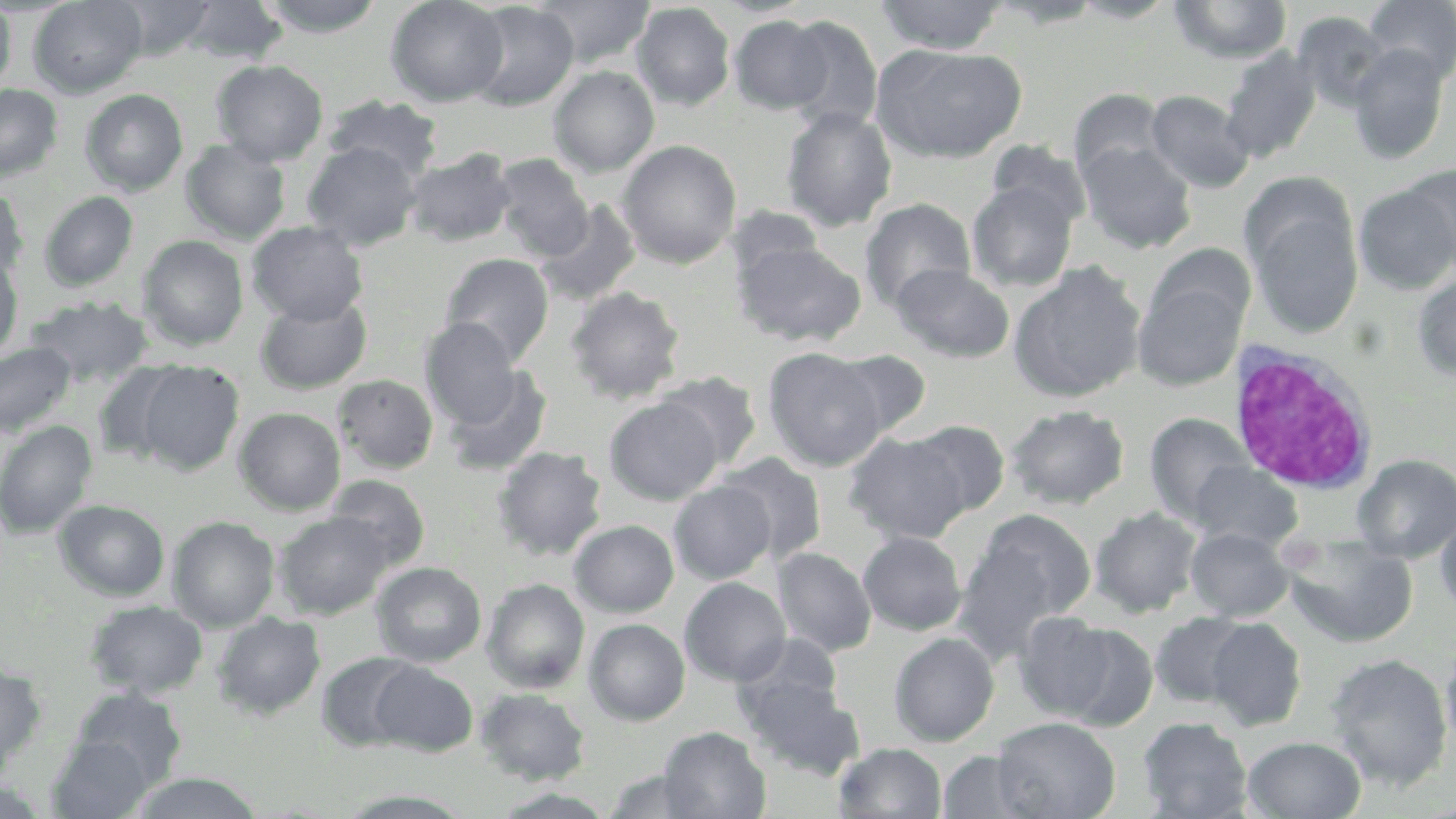
{
  "slide_level_diagnosis": "negative for blood parasites",
  "modality": "optical microscopy",
  "white_blood_cell_locations": "approximate bounding boxes as named x1/y1/x2/y2 corners in pixels: (x1=1226, y1=343, x2=1379, y2=496)",
  "preparation": "thin blood film",
  "stain": "May-Grünwald-Giemsa",
  "image_size": "1456×819 pixels",
  "field_of_view": "single",
  "uninfected_red_blood_cell_locations": "approximate bounding boxes as named x1/y1/x2/y2 corners in pixels: (x1=28, y1=0, x2=147, y2=98), (x1=112, y1=0, x2=218, y2=60), (x1=181, y1=0, x2=289, y2=65), (x1=256, y1=0, x2=386, y2=37), (x1=385, y1=0, x2=509, y2=107), (x1=534, y1=0, x2=655, y2=69), (x1=709, y1=0, x2=815, y2=18), (x1=874, y1=0, x2=1008, y2=54), (x1=1069, y1=0, x2=1181, y2=23), (x1=1361, y1=0, x2=1456, y2=87), (x1=986, y1=1, x2=1106, y2=28), (x1=1169, y1=1, x2=1292, y2=64), (x1=0, y1=2, x2=16, y2=96), (x1=465, y1=2, x2=579, y2=111), (x1=632, y1=2, x2=735, y2=110), (x1=1292, y1=12, x2=1391, y2=111), (x1=729, y1=15, x2=831, y2=114), (x1=783, y1=15, x2=883, y2=135), (x1=872, y1=43, x2=1025, y2=164), (x1=1347, y1=44, x2=1450, y2=165), (x1=1219, y1=46, x2=1322, y2=164), (x1=211, y1=59, x2=329, y2=166), (x1=548, y1=65, x2=659, y2=177), (x1=0, y1=83, x2=63, y2=183), (x1=1069, y1=87, x2=1167, y2=182), (x1=79, y1=89, x2=189, y2=196), (x1=1146, y1=89, x2=1255, y2=194), (x1=323, y1=94, x2=444, y2=182), (x1=780, y1=106, x2=898, y2=232), (x1=180, y1=140, x2=291, y2=244), (x1=302, y1=140, x2=423, y2=250), (x1=617, y1=140, x2=741, y2=269), (x1=986, y1=140, x2=1092, y2=231), (x1=1077, y1=140, x2=1197, y2=254), (x1=405, y1=148, x2=516, y2=247), (x1=491, y1=154, x2=593, y2=263), (x1=1398, y1=164, x2=1456, y2=278), (x1=1354, y1=177, x2=1456, y2=295), (x1=966, y1=180, x2=1078, y2=292), (x1=0, y1=185, x2=29, y2=283), (x1=38, y1=191, x2=138, y2=292), (x1=1247, y1=192, x2=1364, y2=339), (x1=860, y1=198, x2=976, y2=312), (x1=535, y1=199, x2=642, y2=307), (x1=549, y1=200, x2=664, y2=387), (x1=247, y1=221, x2=368, y2=326), (x1=138, y1=236, x2=249, y2=351), (x1=734, y1=239, x2=866, y2=347), (x1=1146, y1=244, x2=1257, y2=339), (x1=0, y1=253, x2=24, y2=362), (x1=439, y1=253, x2=554, y2=365), (x1=1008, y1=262, x2=1146, y2=403), (x1=890, y1=263, x2=1014, y2=363), (x1=1411, y1=273, x2=1456, y2=381), (x1=1134, y1=276, x2=1248, y2=390), (x1=565, y1=286, x2=686, y2=404), (x1=254, y1=295, x2=372, y2=395), (x1=24, y1=296, x2=152, y2=387), (x1=419, y1=318, x2=525, y2=429), (x1=0, y1=341, x2=77, y2=438), (x1=762, y1=347, x2=890, y2=471), (x1=826, y1=349, x2=932, y2=441), (x1=132, y1=360, x2=245, y2=476), (x1=92, y1=362, x2=190, y2=464), (x1=441, y1=365, x2=552, y2=477), (x1=654, y1=372, x2=763, y2=470), (x1=332, y1=374, x2=439, y2=475), (x1=605, y1=398, x2=722, y2=504), (x1=1006, y1=404, x2=1129, y2=509), (x1=233, y1=407, x2=346, y2=515), (x1=1144, y1=412, x2=1252, y2=523), (x1=0, y1=419, x2=98, y2=539), (x1=908, y1=420, x2=1010, y2=516), (x1=846, y1=432, x2=971, y2=543), (x1=492, y1=446, x2=608, y2=562), (x1=718, y1=452, x2=829, y2=565), (x1=1353, y1=454, x2=1456, y2=562), (x1=1189, y1=461, x2=1302, y2=551), (x1=325, y1=474, x2=430, y2=573), (x1=669, y1=480, x2=776, y2=584), (x1=53, y1=499, x2=171, y2=601), (x1=1089, y1=507, x2=1203, y2=617), (x1=975, y1=509, x2=1096, y2=621), (x1=1435, y1=509, x2=1456, y2=620), (x1=274, y1=512, x2=391, y2=619), (x1=166, y1=515, x2=280, y2=632), (x1=569, y1=519, x2=679, y2=617), (x1=1186, y1=527, x2=1294, y2=622), (x1=858, y1=531, x2=967, y2=635), (x1=1284, y1=535, x2=1418, y2=648), (x1=952, y1=539, x2=1065, y2=661), (x1=773, y1=547, x2=877, y2=657), (x1=372, y1=561, x2=486, y2=667), (x1=679, y1=577, x2=791, y2=686), (x1=481, y1=578, x2=590, y2=694), (x1=84, y1=599, x2=208, y2=700), (x1=212, y1=612, x2=326, y2=720), (x1=1014, y1=612, x2=1117, y2=721), (x1=1150, y1=613, x2=1252, y2=709), (x1=1205, y1=617, x2=1306, y2=731), (x1=584, y1=619, x2=690, y2=725), (x1=1057, y1=622, x2=1159, y2=731), (x1=889, y1=632, x2=999, y2=746), (x1=733, y1=634, x2=844, y2=724), (x1=1440, y1=638, x2=1456, y2=754), (x1=316, y1=651, x2=423, y2=752), (x1=1324, y1=653, x2=1453, y2=791), (x1=0, y1=661, x2=47, y2=775), (x1=369, y1=661, x2=478, y2=757), (x1=739, y1=674, x2=864, y2=780), (x1=70, y1=688, x2=188, y2=790), (x1=475, y1=688, x2=591, y2=785), (x1=992, y1=716, x2=1121, y2=819), (x1=1138, y1=716, x2=1253, y2=819), (x1=658, y1=726, x2=771, y2=818), (x1=47, y1=735, x2=155, y2=819), (x1=1242, y1=735, x2=1366, y2=818), (x1=834, y1=742, x2=947, y2=818), (x1=937, y1=751, x2=1038, y2=818), (x1=603, y1=769, x2=708, y2=818), (x1=128, y1=771, x2=264, y2=818), (x1=0, y1=774, x2=52, y2=817), (x1=490, y1=788, x2=617, y2=818), (x1=335, y1=789, x2=476, y2=817)",
  "magnification": "1000x"
}